Comment on the morphology of the red blood cells.
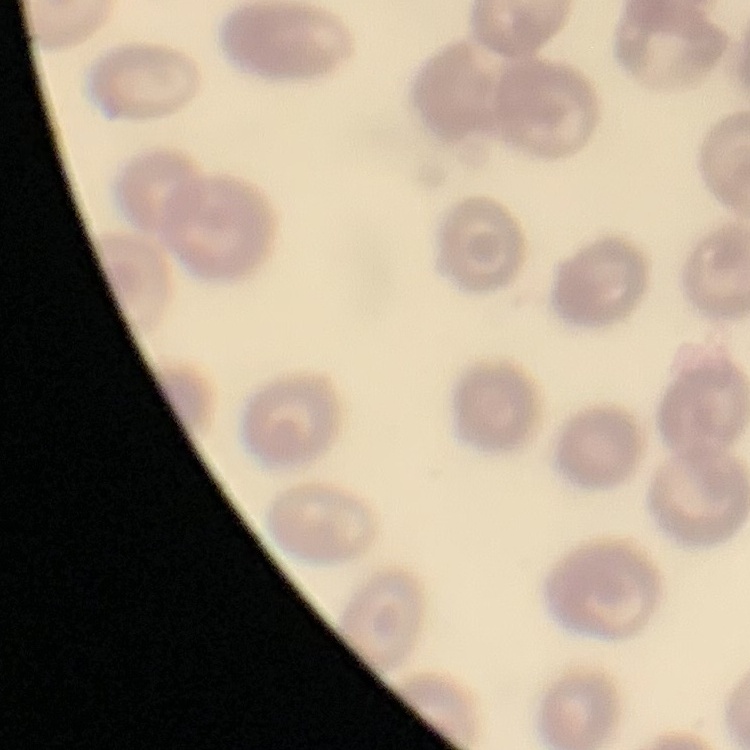

They show no rouleaux formation.

Field's or Giemsa stain. Thin peripheral smear. Square crop of a larger photomicrograph.